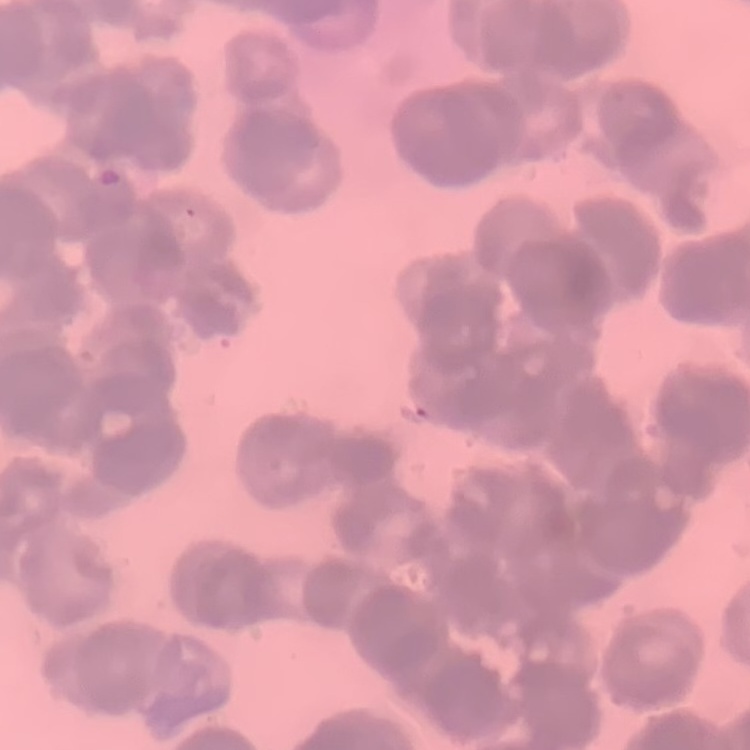

Summary:
  - Red blood cell morphology: rouleaux formation
  - Stain: Field's or Giemsa
  - Preparation: thin peripheral smear
  - Image type: one tile cut from a larger photomicrograph